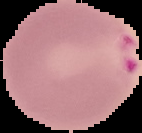

preparation: thin blood film
image_type: segmented cell region with the area outside set to black
image_size: 142×133 pixels
result: malaria parasites detected